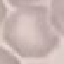
{
  "malaria_status": "uninfected",
  "image_type": "automatically extracted cell patch, resized to 64 × 64 pixels",
  "preparation": "thin smear",
  "capture": "smartphone camera at the microscope eyepiece",
  "stain": "Giemsa"
}